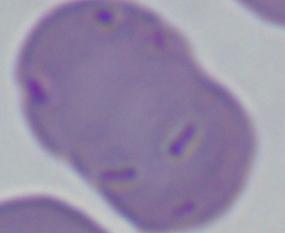
identification = Babesia
magnification = 1000x
modality = photomicrograph